Give the preparation type.
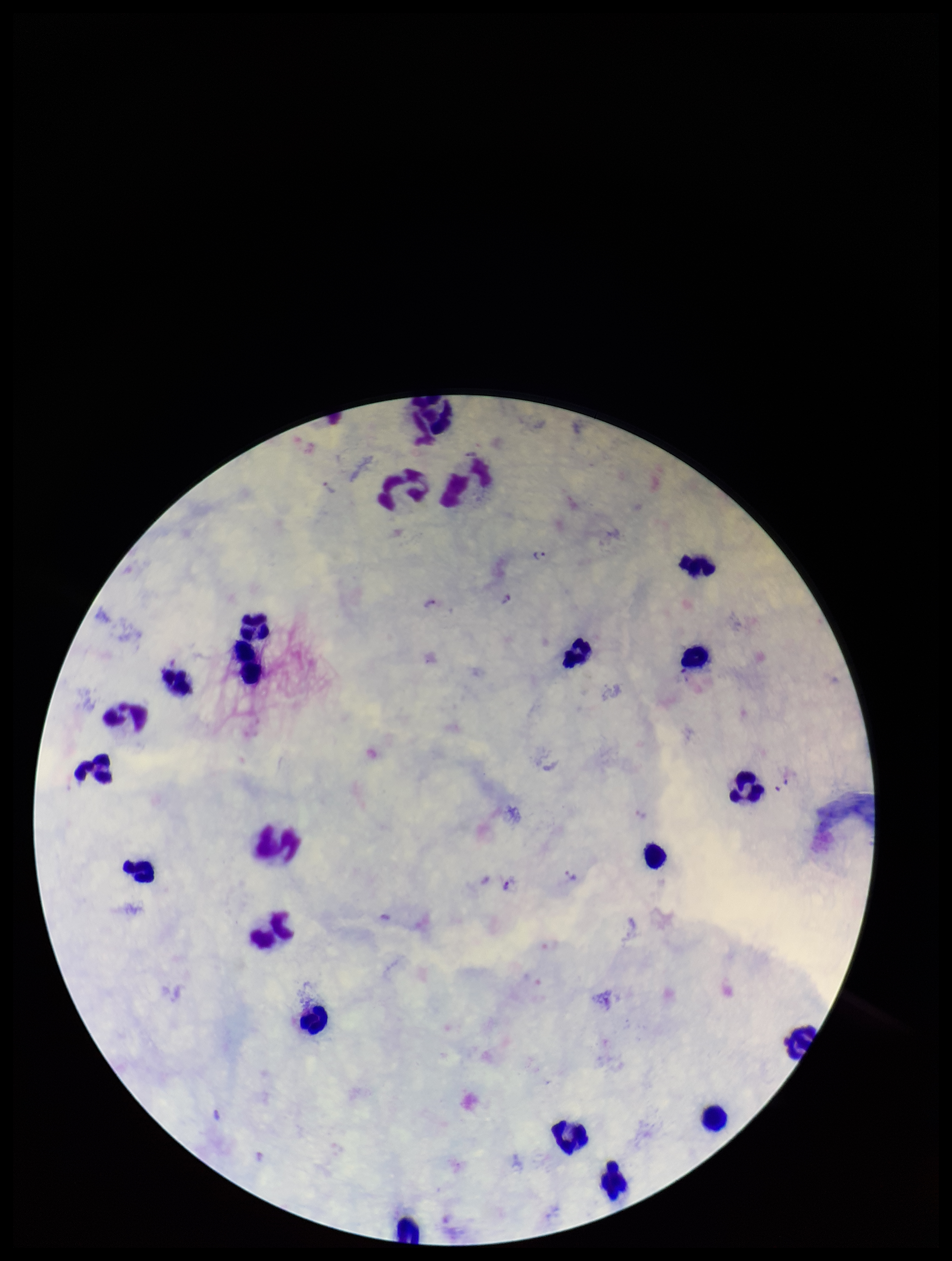
A thick smear.

Summary:
  - Plasmodium parasites: seen
  - Leukocyte count: 21
  - Parasite count: 6
  - Capture: smartphone photograph through the microscope eyepiece
  - Stain: Giemsa
  - Image size: 952×1261 pixels
  - Field of view: single
  - Species reported for this patient: Plasmodium vivax
  - Patient malaria status: infected